Outline every malaria parasite, every leukocyte, and every artifact (stain precipitate or debris).
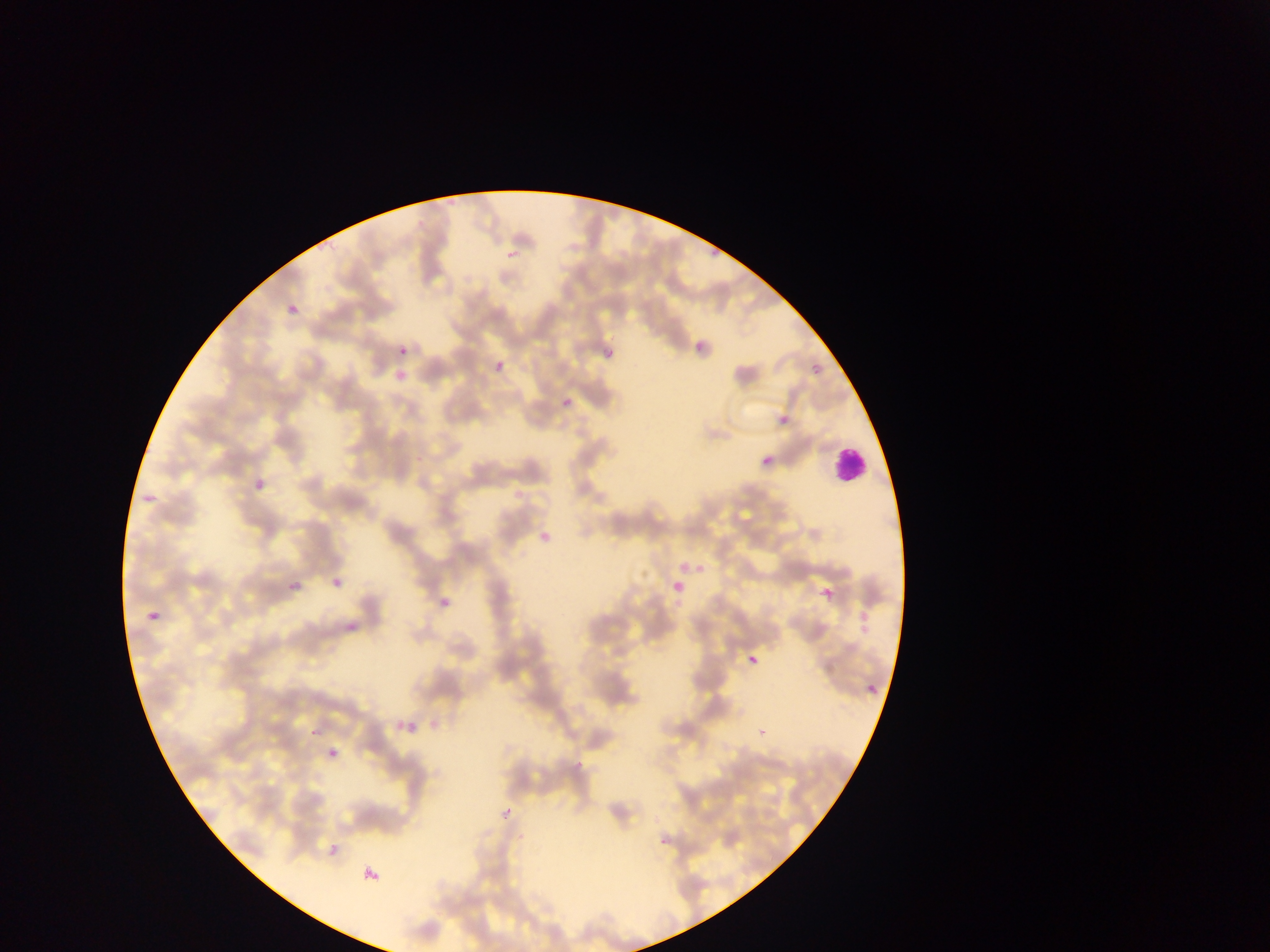

Approximate bounding boxes as left top right bottom in pixels.
Malaria parasites: 501 244 518 262; 278 302 301 321; 691 322 710 357; 600 338 621 360; 398 346 408 355; 495 360 505 370; 812 364 821 373; 563 396 572 406; 780 415 790 425; 762 456 772 465; 249 471 277 501; 137 491 161 503; 531 522 552 550; 674 556 705 576; 325 571 346 596; 816 578 831 603; 287 579 302 593; 667 580 682 598; 429 593 450 613; 138 614 159 627; 343 614 360 635; 744 645 769 669; 865 682 879 696; 394 701 422 736; 755 719 774 736; 305 734 316 747; 324 740 335 761; 497 797 511 830; 652 830 669 850; 322 838 339 857; 359 868 385 886.
Leukocytes: 830 442 869 485.

preparation = thin blood smear
capture = mobile-phone photograph through a microscope
image size = 1270×952 pixels
country = Ghana
field of view = single